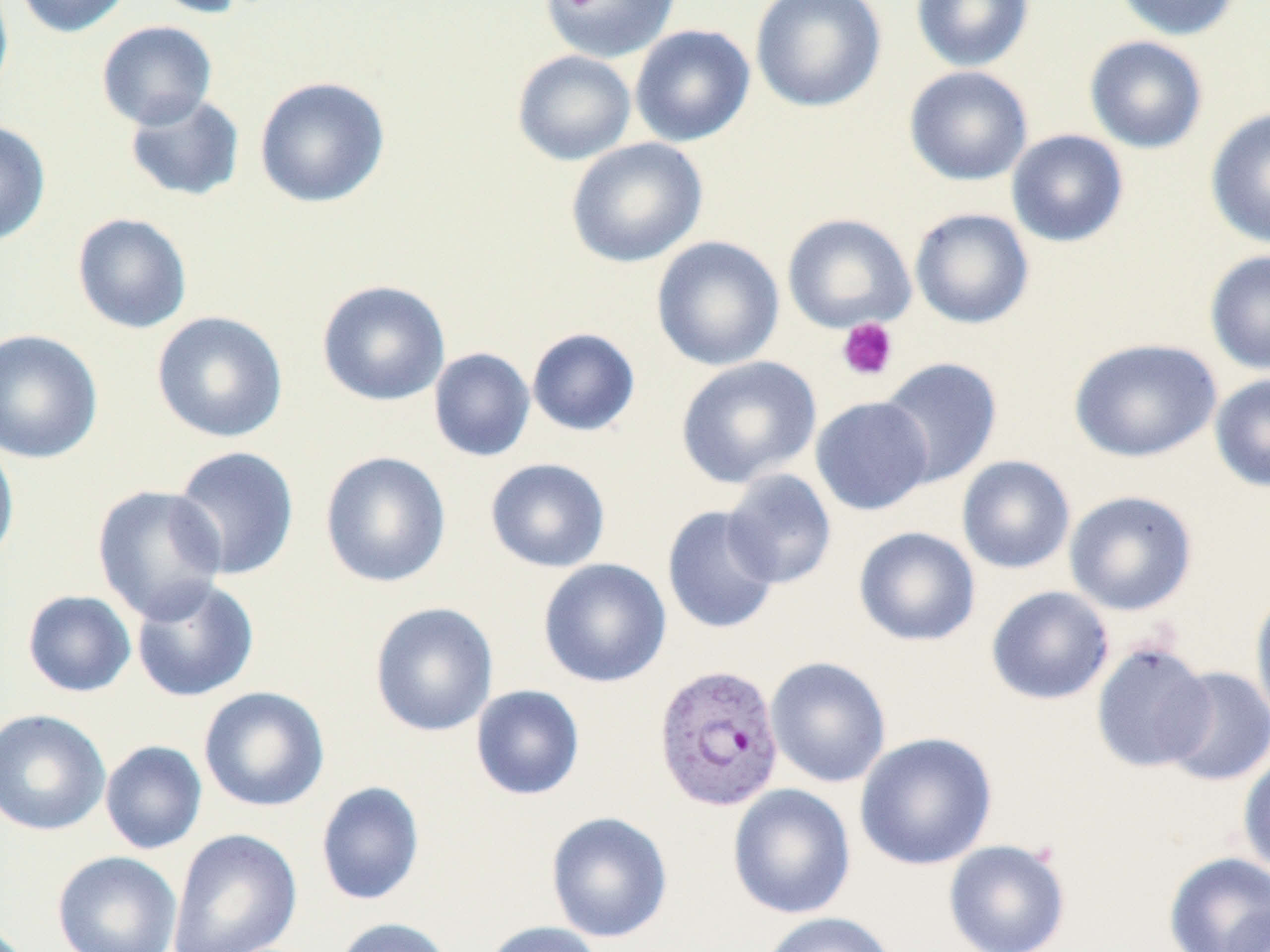

Summary:
  - Coordinate format: approximate bounding boxes as (x1,y1)-(x2,y2) corner pairs in pixels
  - Uninfected red blood cell locations: (0,0)-(14,102), (12,0)-(133,38), (145,0)-(257,19), (539,0)-(681,62), (750,0)-(887,113), (911,0)-(1034,72), (1112,0)-(1241,42), (96,21)-(217,130), (630,24)-(755,147), (1084,35)-(1208,154), (512,49)-(637,166), (904,66)-(1033,186), (254,76)-(390,208), (123,92)-(246,202), (1205,107)-(1270,250), (0,120)-(52,246), (1006,129)-(1129,248), (565,137)-(708,268), (909,208)-(1034,329), (71,212)-(193,334), (782,213)-(916,334), (651,236)-(785,372), (1205,250)-(1270,375), (316,279)-(450,407), (151,310)-(288,443), (527,327)-(641,437), (0,328)-(103,464), (1068,337)-(1223,463), (428,347)-(536,462), (675,355)-(822,489), (878,357)-(1002,488), (1209,373)-(1270,492), (810,395)-(934,515), (0,435)-(20,571), (169,445)-(300,581), (319,451)-(451,588), (956,455)-(1076,574), (484,458)-(610,573), (722,469)-(837,589), (92,484)-(228,623), (1063,490)-(1198,616), (661,505)-(781,635), (853,526)-(981,647), (538,558)-(672,688), (130,577)-(259,703), (986,585)-(1114,705), (1250,588)-(1270,727), (22,590)-(137,698), (369,601)-(498,737), (1090,640)-(1216,774), (765,656)-(891,788), (1160,666)-(1270,786), (470,685)-(585,801), (198,686)-(330,813), (0,708)-(111,837), (854,732)-(997,870), (100,740)-(207,855), (1237,752)-(1270,878), (315,781)-(425,906), (727,783)-(856,919), (546,811)-(673,943), (166,828)-(302,952), (943,839)-(1071,952), (51,850)-(183,952), (1163,851)-(1270,952), (1219,902)-(1270,952), (755,911)-(900,952), (332,917)-(456,952), (480,920)-(606,952)
  - Plasmodium vivax-infected red blood cell locations: (653,662)-(785,812)
  - Platelet locations: (836,317)-(898,382)
  - Slide-level diagnosis: Plasmodium vivax
  - Image size: 1270×952 pixels
  - Modality: light microscopy
  - Field of view: one of a larger specimen
  - Preparation: thin blood smear
  - Stain: May-Grünwald-Giemsa
  - Magnification: 1000x